Locate every Plasmodium ovale-infected red blood cell.
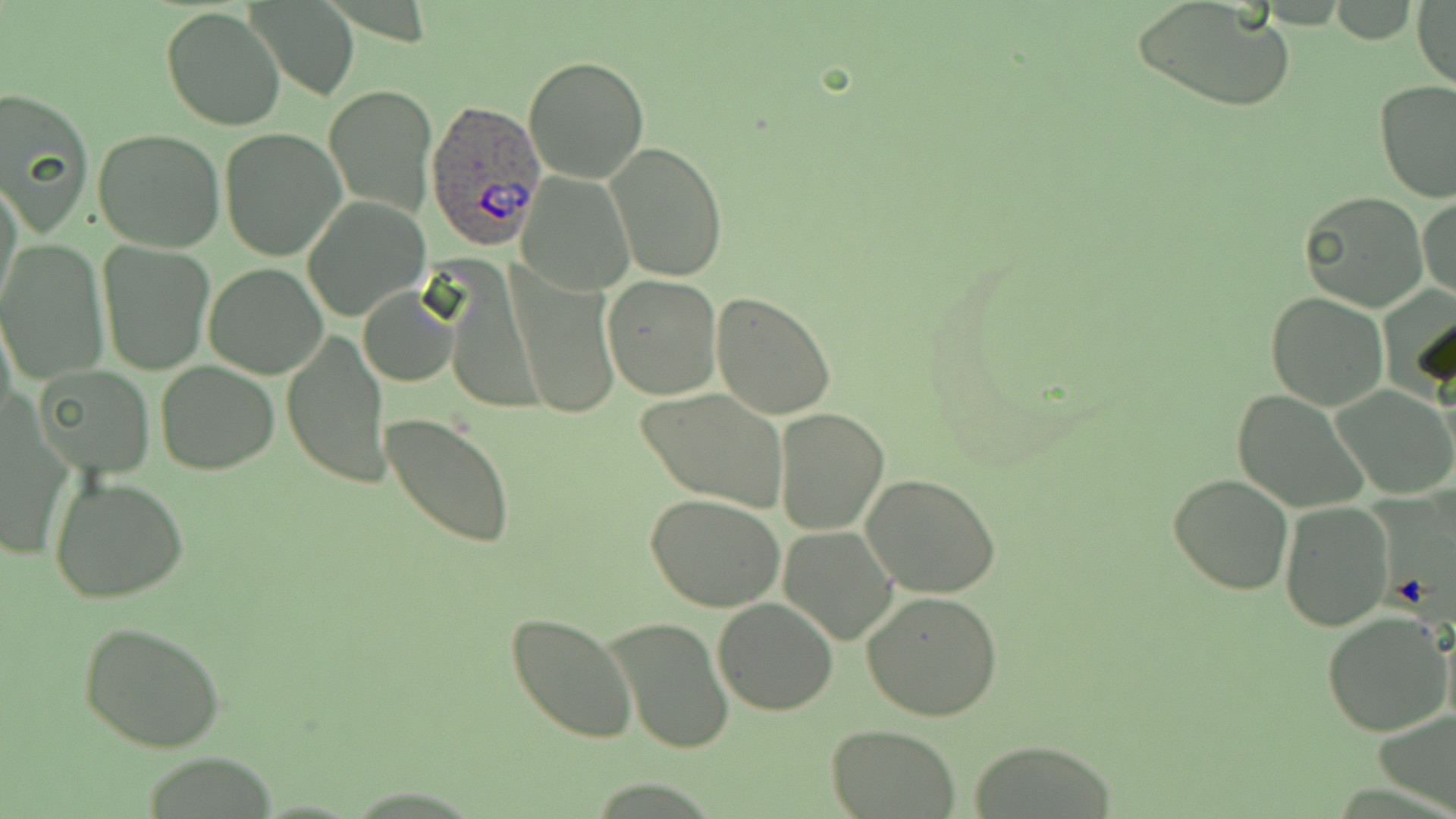
Approximate bounding boxes as named x1/y1/x2/y2 corners in pixels.
Plasmodium ovale-infected red blood cells: (x1=425, y1=97, x2=547, y2=251).

Summary:
  - Uninfected red blood cell locations: (x1=1130, y1=1, x2=1296, y2=113), (x1=1412, y1=2, x2=1455, y2=90), (x1=248, y1=3, x2=359, y2=100), (x1=162, y1=6, x2=286, y2=130), (x1=525, y1=56, x2=649, y2=184), (x1=1374, y1=81, x2=1456, y2=204), (x1=1, y1=84, x2=95, y2=235), (x1=325, y1=86, x2=437, y2=217), (x1=92, y1=127, x2=226, y2=252), (x1=220, y1=127, x2=347, y2=263), (x1=604, y1=142, x2=728, y2=285), (x1=518, y1=173, x2=635, y2=296), (x1=1, y1=177, x2=22, y2=316), (x1=1298, y1=191, x2=1429, y2=313), (x1=302, y1=194, x2=431, y2=323), (x1=1417, y1=194, x2=1456, y2=304), (x1=0, y1=236, x2=109, y2=383), (x1=98, y1=242, x2=214, y2=374), (x1=203, y1=264, x2=329, y2=379), (x1=508, y1=264, x2=619, y2=421), (x1=602, y1=274, x2=722, y2=399), (x1=358, y1=285, x2=458, y2=387), (x1=1265, y1=291, x2=1390, y2=411), (x1=711, y1=292, x2=836, y2=420), (x1=282, y1=330, x2=390, y2=486), (x1=154, y1=361, x2=280, y2=475), (x1=33, y1=365, x2=154, y2=478), (x1=1331, y1=385, x2=1455, y2=499), (x1=636, y1=389, x2=789, y2=509), (x1=1232, y1=390, x2=1368, y2=513), (x1=773, y1=408, x2=889, y2=535), (x1=382, y1=410, x2=517, y2=549), (x1=1168, y1=471, x2=1293, y2=594), (x1=862, y1=473, x2=1002, y2=598), (x1=48, y1=476, x2=191, y2=606), (x1=645, y1=492, x2=786, y2=611), (x1=1280, y1=503, x2=1394, y2=629), (x1=778, y1=526, x2=898, y2=643), (x1=862, y1=591, x2=1006, y2=720), (x1=713, y1=597, x2=836, y2=715), (x1=1322, y1=611, x2=1454, y2=738), (x1=506, y1=612, x2=638, y2=742), (x1=606, y1=617, x2=735, y2=753), (x1=78, y1=622, x2=226, y2=754), (x1=1376, y1=705, x2=1456, y2=811), (x1=826, y1=724, x2=961, y2=818), (x1=971, y1=738, x2=1118, y2=818)
  - Slide-level diagnosis: Plasmodium ovale
  - Image size: 1456×819 pixels
  - Preparation: thin blood film
  - Field of view: single
  - Stain: May-Grünwald-Giemsa
  - Magnification: 1000x
  - Modality: light microscopy